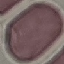
Result: no malaria parasites detected. Thin blood film. Photographed with a smartphone camera at the microscope eyepiece. Cell patch, automatically extracted from a larger field of view and resized to 64 × 64 pixels. Giemsa stain.